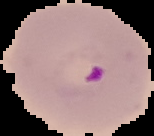 From a thin blood film. Image is 154×136 pixels. Cell region segmented out of the field of view; the surrounding area is masked to black. Malaria status: parasitized.